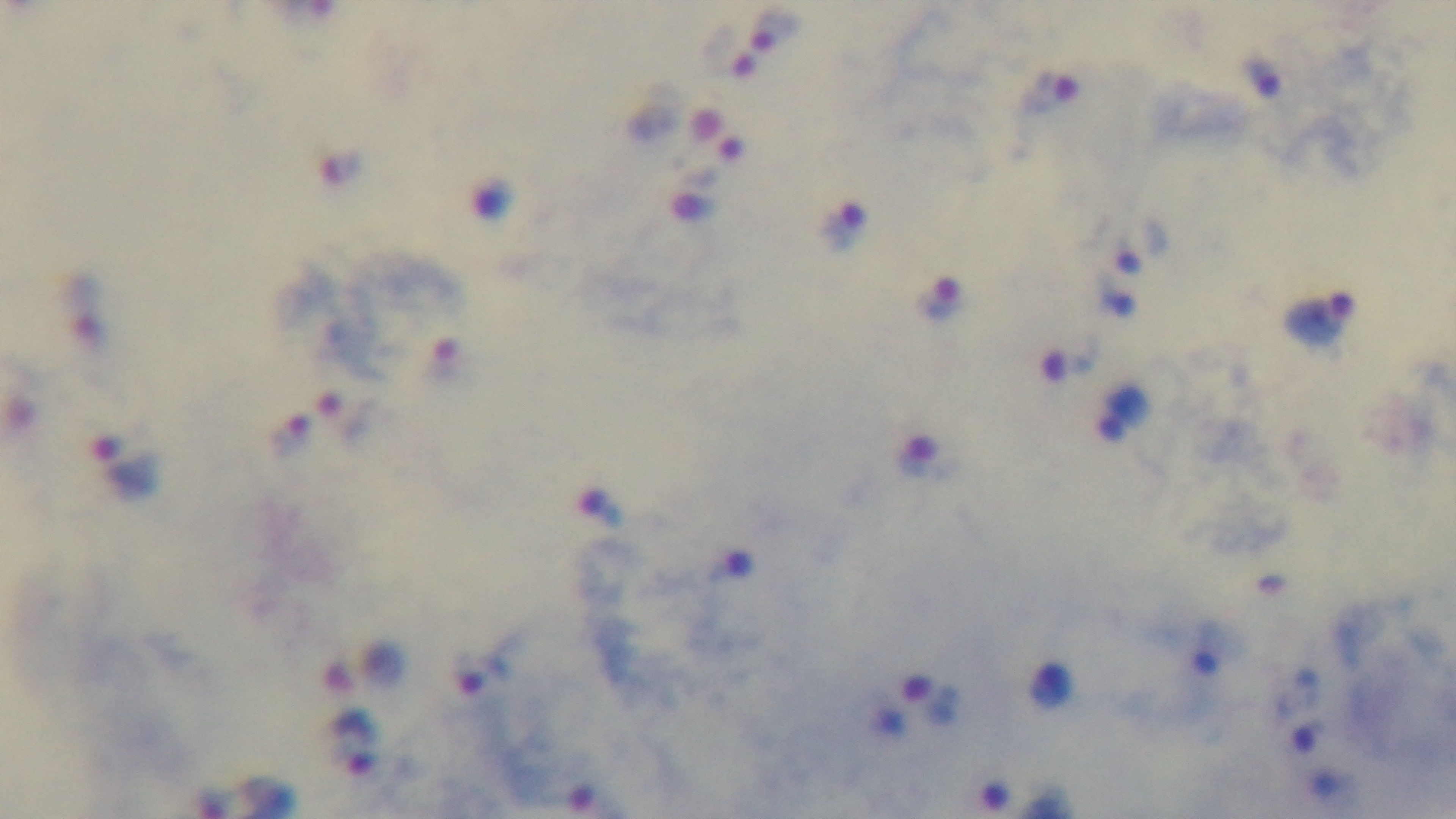
objective = 100x oil immersion
stain = Giemsa
malaria status = infected
preparation = thick blood film
modality = light microscopy
capture = mounted 4K digital camera
field of view = one from the slide